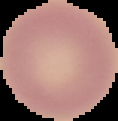

Summary:
  - Preparation: thin blood smear
  - Image size: 118×121 pixels
  - Malaria status: uninfected
  - Image type: cell region segmented out of the field of view; surrounding area masked to black